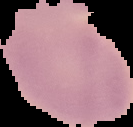 From a thin blood smear. Malaria status: uninfected. Image is 133×127 pixels. Cell region segmented out of the field of view; the surrounding area is masked to black.